Report the malaria status of this cell.
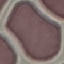
It is uninfected.

Summary:
  - Image type: cell patch, automatically extracted from a larger field of view and resized to 64 × 64 pixels
  - Preparation: thin smear
  - Capture: smartphone through the microscope eyepiece
  - Stain: Giemsa